Classify this cell by malaria status.
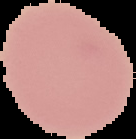
It is uninfected.

From a thin blood film. Segmented cell region on a black background. Image is 136×139 pixels.